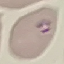
{
  "result": "malaria parasites identified",
  "preparation": "thin smear",
  "image_type": "automatically extracted cell patch, resized to 64 × 64 pixels",
  "stain": "Giemsa",
  "capture": "smartphone through the microscope eyepiece"
}